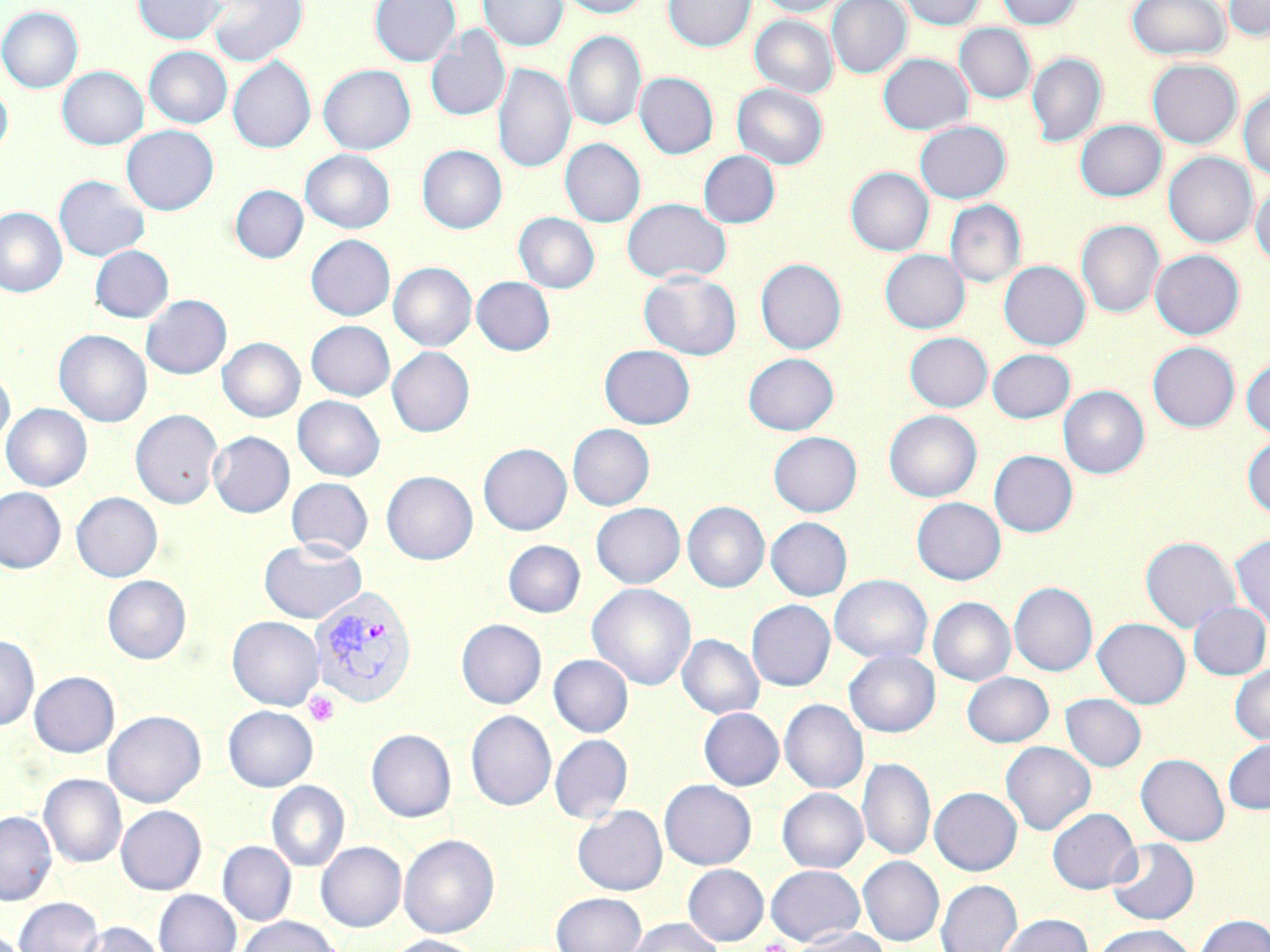

Summary:
  - Coordinate format: approximate bounding boxes as named x1/y1/x2/y2 corners in pixels
  - Platelet locations: (x1=304, y1=690, x2=339, y2=726), (x1=762, y1=937, x2=791, y2=952)
  - Plasmodium vivax-infected red blood cell locations: (x1=309, y1=586, x2=417, y2=708)
  - Uninfected red blood cell locations: (x1=133, y1=0, x2=227, y2=44), (x1=207, y1=0, x2=308, y2=66), (x1=370, y1=0, x2=461, y2=66), (x1=478, y1=0, x2=568, y2=52), (x1=557, y1=0, x2=651, y2=18), (x1=663, y1=0, x2=755, y2=52), (x1=757, y1=0, x2=849, y2=17), (x1=826, y1=0, x2=911, y2=78), (x1=899, y1=0, x2=986, y2=30), (x1=996, y1=0, x2=1082, y2=30), (x1=1126, y1=0, x2=1231, y2=60), (x1=1224, y1=0, x2=1270, y2=40), (x1=0, y1=6, x2=83, y2=93), (x1=750, y1=15, x2=837, y2=98), (x1=955, y1=23, x2=1035, y2=103), (x1=425, y1=26, x2=510, y2=122), (x1=563, y1=31, x2=647, y2=131), (x1=144, y1=46, x2=232, y2=128), (x1=1027, y1=52, x2=1107, y2=147), (x1=878, y1=53, x2=972, y2=135), (x1=228, y1=56, x2=316, y2=153), (x1=1147, y1=59, x2=1242, y2=148), (x1=492, y1=62, x2=575, y2=174), (x1=318, y1=64, x2=416, y2=154), (x1=57, y1=66, x2=148, y2=150), (x1=634, y1=72, x2=718, y2=159), (x1=0, y1=81, x2=12, y2=159), (x1=732, y1=83, x2=828, y2=169), (x1=1239, y1=88, x2=1270, y2=180), (x1=1075, y1=119, x2=1166, y2=201), (x1=915, y1=120, x2=1011, y2=204), (x1=122, y1=125, x2=219, y2=215), (x1=560, y1=138, x2=645, y2=227), (x1=417, y1=144, x2=506, y2=233), (x1=300, y1=149, x2=395, y2=233), (x1=698, y1=150, x2=780, y2=228), (x1=1164, y1=152, x2=1257, y2=248), (x1=846, y1=167, x2=933, y2=256), (x1=54, y1=175, x2=149, y2=261), (x1=1250, y1=182, x2=1270, y2=268), (x1=230, y1=185, x2=308, y2=263), (x1=621, y1=198, x2=732, y2=284), (x1=945, y1=201, x2=1025, y2=288), (x1=0, y1=207, x2=67, y2=297), (x1=514, y1=212, x2=599, y2=293), (x1=1076, y1=220, x2=1164, y2=318), (x1=306, y1=234, x2=395, y2=320), (x1=89, y1=245, x2=174, y2=322), (x1=880, y1=249, x2=969, y2=334), (x1=1150, y1=249, x2=1244, y2=339), (x1=755, y1=258, x2=847, y2=354), (x1=999, y1=260, x2=1090, y2=350), (x1=389, y1=262, x2=477, y2=351), (x1=639, y1=270, x2=742, y2=360), (x1=471, y1=276, x2=555, y2=355), (x1=141, y1=295, x2=231, y2=379), (x1=306, y1=320, x2=395, y2=401), (x1=54, y1=329, x2=152, y2=427), (x1=905, y1=332, x2=992, y2=412), (x1=218, y1=337, x2=305, y2=422), (x1=1148, y1=342, x2=1240, y2=432), (x1=599, y1=344, x2=695, y2=429), (x1=387, y1=347, x2=474, y2=437), (x1=987, y1=349, x2=1075, y2=423), (x1=743, y1=353, x2=839, y2=435), (x1=1242, y1=358, x2=1270, y2=439), (x1=0, y1=367, x2=15, y2=450), (x1=1059, y1=386, x2=1149, y2=479), (x1=293, y1=395, x2=385, y2=481), (x1=1, y1=403, x2=92, y2=491), (x1=130, y1=409, x2=223, y2=509), (x1=884, y1=410, x2=982, y2=502), (x1=568, y1=424, x2=655, y2=510), (x1=208, y1=431, x2=294, y2=517), (x1=768, y1=431, x2=862, y2=517), (x1=1243, y1=435, x2=1270, y2=520), (x1=478, y1=443, x2=572, y2=535), (x1=989, y1=450, x2=1078, y2=537), (x1=381, y1=471, x2=478, y2=564), (x1=286, y1=477, x2=373, y2=558), (x1=0, y1=486, x2=66, y2=573), (x1=71, y1=492, x2=162, y2=582), (x1=912, y1=497, x2=1006, y2=585), (x1=682, y1=501, x2=770, y2=593), (x1=591, y1=502, x2=685, y2=588), (x1=766, y1=517, x2=852, y2=601), (x1=1230, y1=534, x2=1270, y2=630), (x1=1140, y1=536, x2=1240, y2=633), (x1=259, y1=538, x2=367, y2=623), (x1=503, y1=540, x2=585, y2=617), (x1=103, y1=575, x2=191, y2=663), (x1=830, y1=575, x2=932, y2=663), (x1=1009, y1=582, x2=1097, y2=676), (x1=587, y1=583, x2=696, y2=690), (x1=928, y1=597, x2=1015, y2=686), (x1=746, y1=600, x2=835, y2=691), (x1=1188, y1=601, x2=1270, y2=679), (x1=227, y1=616, x2=324, y2=710), (x1=1093, y1=618, x2=1190, y2=709), (x1=456, y1=619, x2=546, y2=709), (x1=677, y1=634, x2=764, y2=719), (x1=0, y1=635, x2=39, y2=730), (x1=844, y1=649, x2=940, y2=737), (x1=549, y1=654, x2=633, y2=737), (x1=1230, y1=664, x2=1270, y2=745), (x1=28, y1=671, x2=119, y2=757), (x1=962, y1=671, x2=1054, y2=747), (x1=1060, y1=693, x2=1146, y2=771), (x1=779, y1=699, x2=868, y2=794), (x1=223, y1=706, x2=318, y2=792), (x1=699, y1=708, x2=784, y2=790), (x1=103, y1=710, x2=206, y2=807), (x1=466, y1=710, x2=556, y2=810), (x1=366, y1=728, x2=457, y2=821), (x1=550, y1=734, x2=632, y2=823), (x1=1223, y1=737, x2=1270, y2=814), (x1=1000, y1=741, x2=1096, y2=835), (x1=1136, y1=753, x2=1229, y2=846), (x1=857, y1=757, x2=935, y2=861), (x1=39, y1=774, x2=127, y2=867), (x1=659, y1=779, x2=756, y2=869), (x1=266, y1=781, x2=350, y2=872), (x1=929, y1=787, x2=1022, y2=875), (x1=777, y1=788, x2=868, y2=873), (x1=116, y1=805, x2=206, y2=895), (x1=573, y1=805, x2=667, y2=895), (x1=1047, y1=807, x2=1141, y2=894), (x1=0, y1=811, x2=56, y2=905), (x1=399, y1=833, x2=500, y2=938), (x1=1107, y1=838, x2=1199, y2=925), (x1=217, y1=841, x2=297, y2=925), (x1=316, y1=841, x2=406, y2=931), (x1=858, y1=856, x2=944, y2=945), (x1=682, y1=864, x2=769, y2=946), (x1=766, y1=865, x2=865, y2=945), (x1=936, y1=880, x2=1022, y2=952), (x1=154, y1=889, x2=241, y2=952), (x1=551, y1=892, x2=647, y2=952), (x1=14, y1=896, x2=103, y2=952), (x1=998, y1=913, x2=1094, y2=952), (x1=1195, y1=914, x2=1270, y2=952), (x1=236, y1=916, x2=341, y2=952), (x1=626, y1=918, x2=724, y2=952), (x1=74, y1=921, x2=164, y2=952), (x1=1090, y1=924, x2=1197, y2=952), (x1=791, y1=927, x2=891, y2=952), (x1=383, y1=935, x2=486, y2=952)
  - Slide-level diagnosis: Plasmodium vivax
  - Modality: light microscopy
  - Preparation: thin blood film
  - Magnification: 1000x
  - Stain: May-Grünwald-Giemsa
  - Image size: 1270×952 pixels
  - Field of view: single